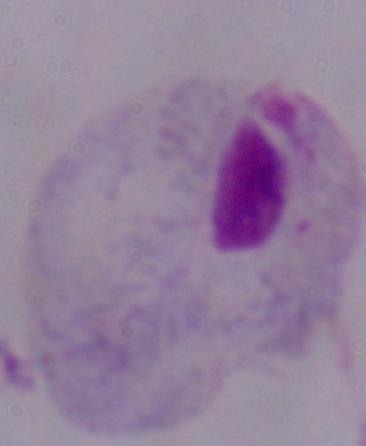
Summary:
  - Modality: photomicrograph
  - Magnification: 1000x
  - Identification: trichomonad